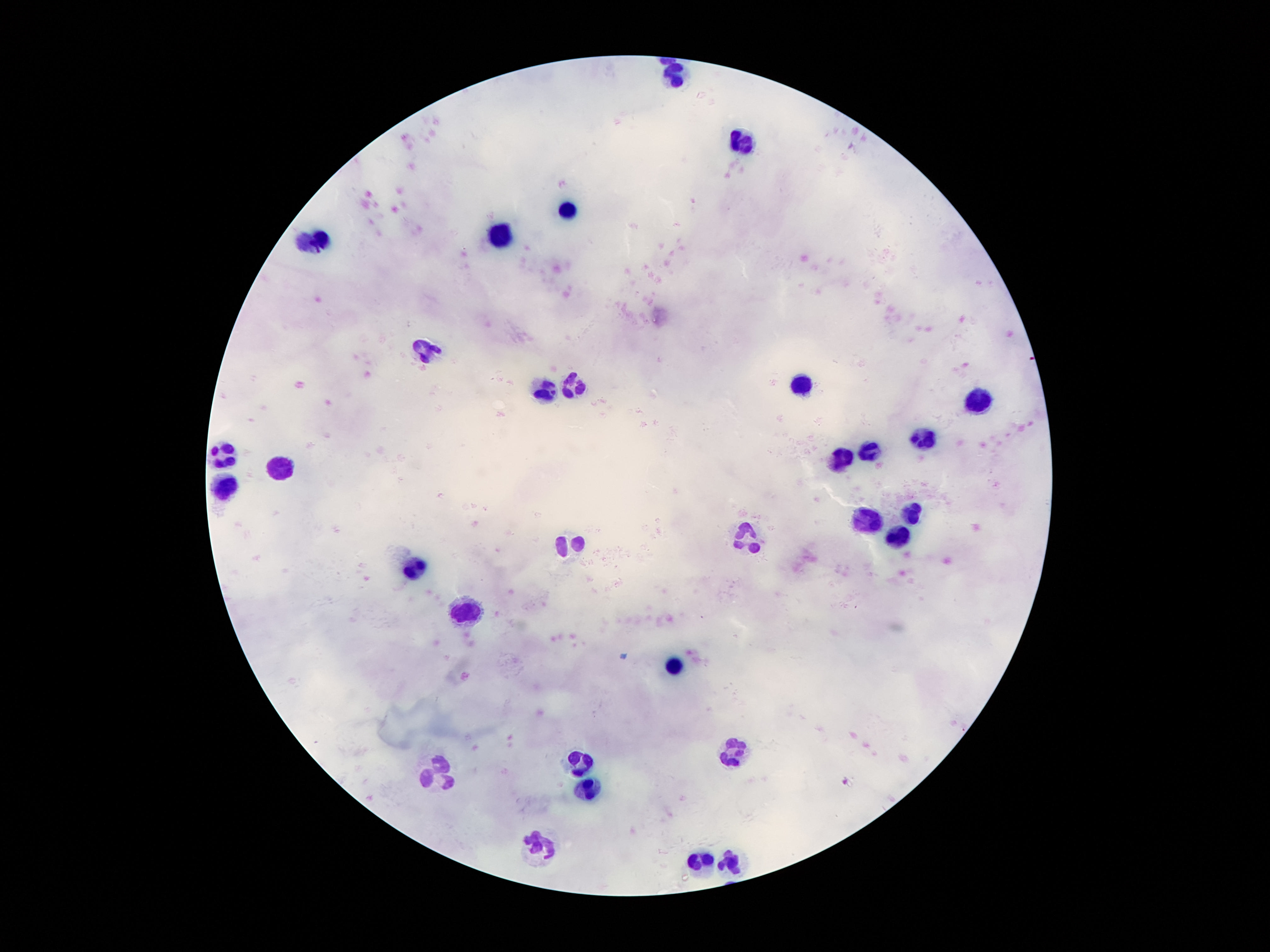

Approximate centers as {x, y} in pixels. Leukocyte locations: {674, 75}, {735, 143}, {567, 210}, {322, 236}, {500, 236}, {301, 243}, {422, 351}, {801, 383}, {574, 384}, {545, 392}, {975, 400}, {920, 441}, {870, 452}, {223, 454}, {842, 462}, {281, 466}, {225, 486}, {911, 512}, {862, 523}, {750, 536}, {899, 542}, {569, 544}, {416, 567}, {469, 612}, {672, 663}, {733, 753}, {578, 759}, {436, 773}, {590, 792}, {541, 845}, {700, 862}, {729, 862}. Single field of view. Photographed through the microscope eyepiece with a smartphone camera. Patient malaria status: negative. Thick blood smear. 100x magnification. Image is 1270×952 pixels. Giemsa-stained preparation.